Point out each Plasmodium parasite.
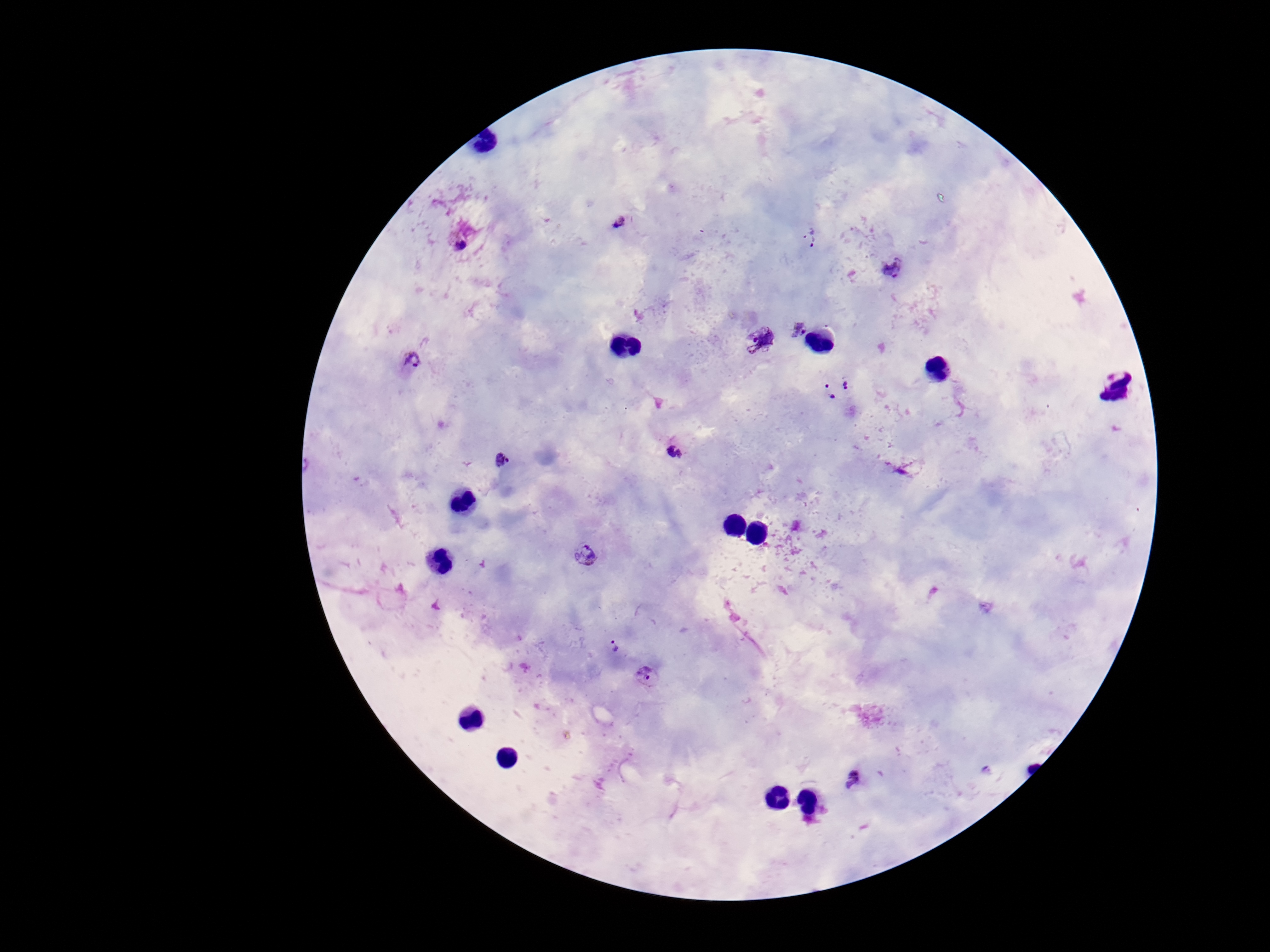
Approximate centers as [x, y] in pixels.
Plasmodium parasites: [619, 222], [809, 239], [460, 244], [893, 266], [800, 330], [761, 340], [411, 360], [848, 383], [1119, 387], [829, 392], [676, 453], [502, 460], [585, 555], [612, 647], [645, 678], [857, 781].

capture = smartphone camera through the microscope eyepiece
field of view = single
preparation = thick blood film
magnification = 100x
stain = Giemsa
patient malaria status = positive
image size = 1270×952 pixels